Outline platelets.
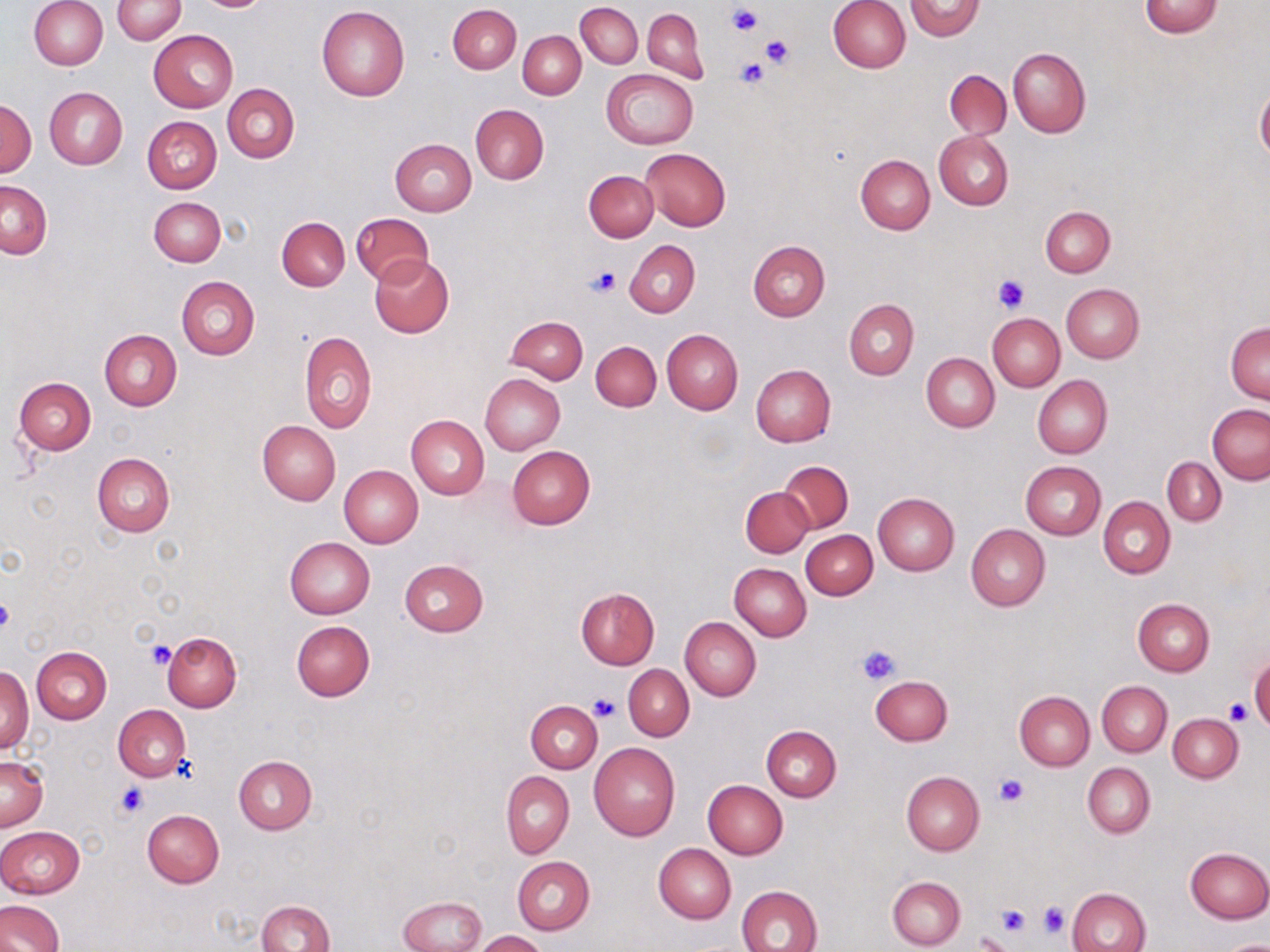
Approximate bounding boxes as [x1, y1, x2, y2] in pixels.
Platelets: [726, 3, 763, 36], [760, 35, 795, 67], [733, 58, 769, 90], [587, 266, 619, 298], [992, 275, 1031, 313], [0, 595, 15, 637], [147, 640, 175, 667], [858, 643, 901, 685], [589, 695, 619, 722], [1225, 699, 1251, 723], [995, 773, 1029, 806], [114, 783, 147, 820], [1037, 900, 1067, 938], [997, 903, 1030, 936], [974, 931, 1014, 952].

slide-level diagnosis = no evidence of blood parasites
modality = optical microscopy
preparation = thin blood smear
stain = May-Grünwald-Giemsa
magnification = 1000x
image size = 1270×952 pixels
uninfected red blood cell locations = approximate bounding boxes as [x1, y1, x2, y2] in pixels: [907, 0, 985, 41], [28, 1, 107, 69], [112, 1, 185, 42], [828, 1, 910, 73], [1138, 1, 1223, 37], [575, 2, 642, 68], [449, 4, 521, 74], [316, 6, 410, 101], [642, 8, 706, 82], [149, 29, 238, 112], [519, 31, 585, 99], [1008, 48, 1091, 137], [602, 69, 699, 149], [945, 70, 1011, 139], [223, 84, 299, 162], [44, 87, 127, 170], [1256, 87, 1270, 164], [1, 98, 36, 178], [471, 104, 548, 184], [142, 116, 222, 193], [934, 131, 1014, 210], [389, 139, 475, 216], [642, 148, 731, 230], [856, 154, 934, 235], [584, 170, 658, 242], [1, 180, 52, 258], [149, 197, 225, 266], [1040, 207, 1113, 277], [352, 212, 434, 287], [277, 216, 349, 291], [624, 240, 700, 317], [748, 241, 830, 321], [370, 253, 455, 338], [177, 276, 259, 361], [1061, 283, 1144, 363], [845, 299, 918, 379], [988, 313, 1065, 392], [505, 315, 587, 384], [1226, 321, 1270, 403], [99, 329, 180, 410], [662, 329, 743, 414], [300, 331, 377, 433], [590, 341, 661, 411], [921, 353, 1000, 432], [750, 365, 836, 447], [480, 373, 565, 454], [1033, 375, 1112, 459], [14, 377, 95, 455], [1208, 405, 1269, 483], [406, 415, 489, 499], [257, 420, 340, 506], [507, 445, 596, 529], [92, 453, 174, 537], [1162, 456, 1225, 525], [779, 461, 853, 533], [1020, 461, 1106, 540], [339, 465, 423, 547], [741, 485, 814, 558], [872, 493, 959, 575], [1099, 496, 1175, 578], [966, 523, 1051, 611], [801, 530, 877, 599], [285, 536, 375, 619], [399, 560, 489, 637], [730, 563, 811, 640], [574, 587, 659, 670], [1132, 599, 1214, 676], [680, 617, 761, 701], [291, 621, 375, 701], [162, 631, 241, 712], [32, 647, 112, 724], [1250, 657, 1270, 730], [1, 664, 33, 755], [624, 665, 693, 742], [871, 675, 953, 745], [1097, 681, 1171, 756], [1014, 690, 1095, 771], [526, 700, 603, 773], [113, 705, 191, 782], [1168, 715, 1242, 783], [762, 726, 841, 802], [588, 742, 680, 840], [0, 755, 48, 832], [233, 755, 316, 833], [1082, 761, 1155, 838], [500, 771, 574, 858], [901, 771, 984, 856], [703, 781, 787, 859], [142, 809, 225, 887], [0, 826, 86, 899], [653, 844, 736, 924], [1185, 847, 1270, 923], [512, 856, 594, 934], [886, 875, 966, 950], [738, 885, 823, 952], [1067, 887, 1151, 951], [397, 895, 485, 952], [0, 900, 65, 952], [257, 900, 334, 952], [473, 930, 548, 952], [1215, 939, 1270, 952]
field of view = single